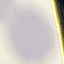 Malaria status: uninfected. Acquired by smartphone through the microscope eyepiece. Thin smear of blood. Automatically extracted cell patch, resized to 64 × 64 pixels. Giemsa stain.